Identify the parasite.
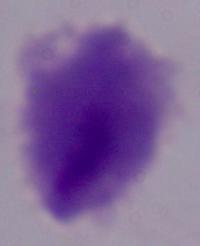
A trichomonad.

Summary:
  - Modality: micrograph
  - Magnification: 1000x